State the preparation type.
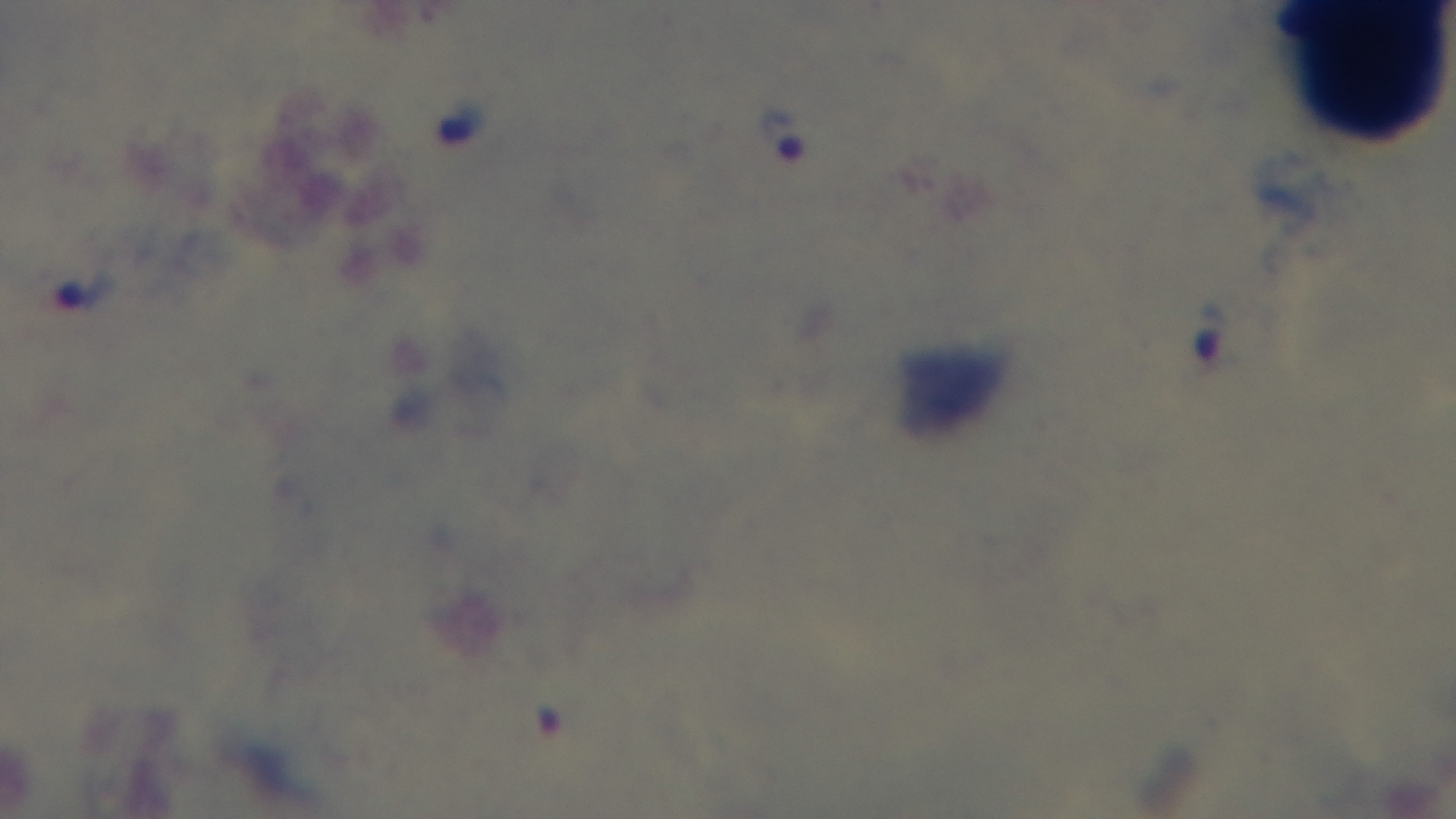
A thick smear.

malaria status = infected
objective = 100x oil immersion
capture = mounted 4K digital camera
stain = Giemsa
modality = light microscopy
field of view = single